Name the cell type shown.
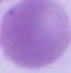

This is an erythrocyte.

modality: micrograph
magnification: 1000x